Give the extent of all uninfected red blood cells.
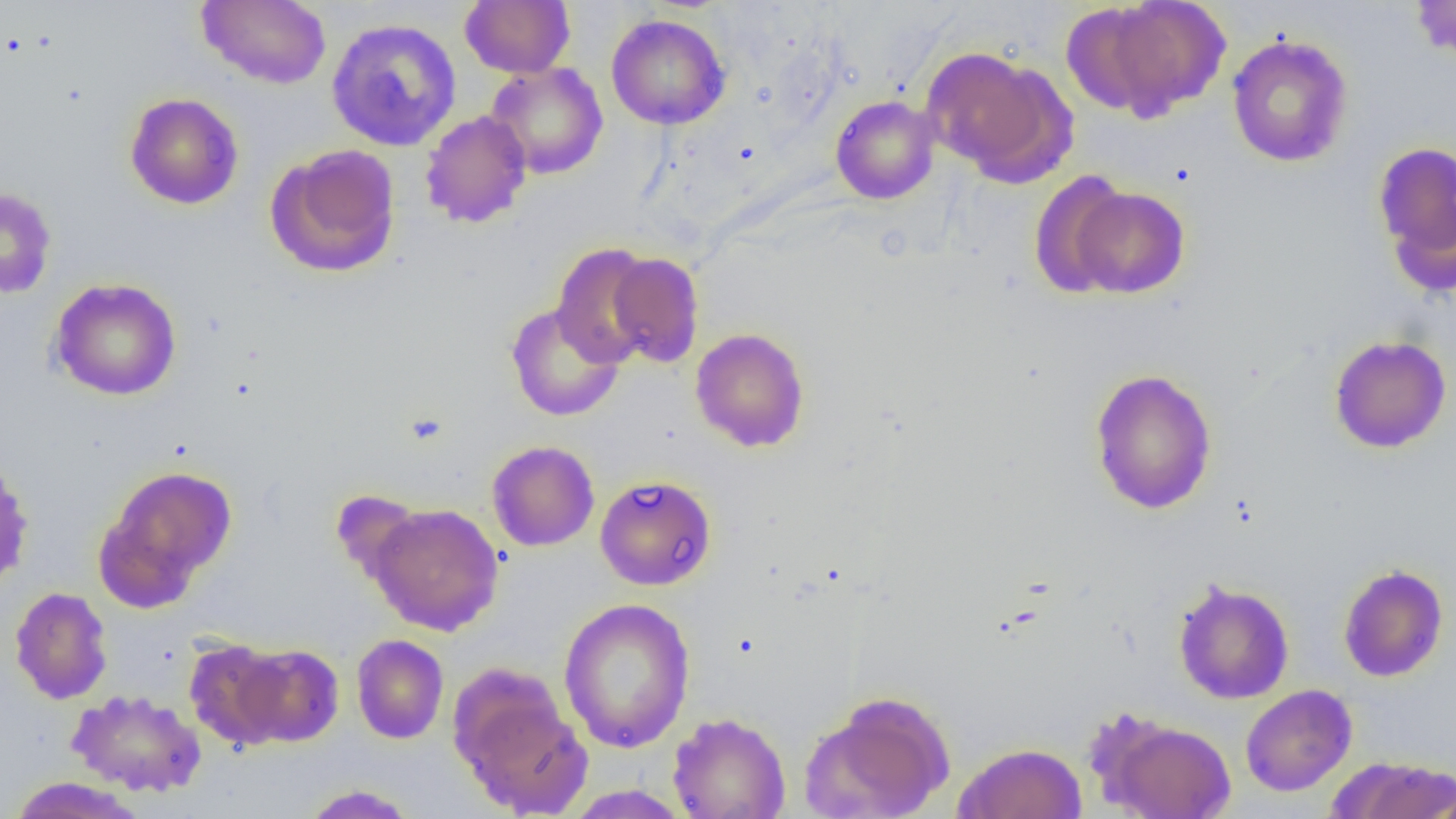
Approximate bounding boxes as (x1, y1, x2, y2) in pixels.
Uninfected red blood cells: (197, 0, 331, 89), (460, 0, 575, 78), (1081, 0, 1233, 121), (1410, 0, 1456, 63), (606, 14, 731, 130), (326, 17, 462, 151), (1226, 33, 1354, 168), (921, 46, 1073, 184), (485, 62, 608, 180), (125, 92, 243, 210), (830, 95, 940, 205), (420, 110, 532, 228), (1372, 139, 1456, 291), (266, 144, 402, 278), (1029, 171, 1135, 299), (1068, 186, 1190, 298), (0, 187, 57, 299), (551, 243, 660, 367), (603, 251, 705, 368), (49, 277, 182, 401), (505, 301, 625, 422), (690, 327, 810, 453), (1328, 335, 1452, 454), (1089, 367, 1217, 515), (487, 440, 600, 551), (0, 459, 34, 592), (95, 464, 237, 609), (594, 474, 717, 591), (330, 489, 431, 594), (367, 503, 504, 635), (1338, 563, 1449, 682), (1173, 579, 1295, 705), (10, 587, 113, 705), (558, 598, 696, 753), (352, 635, 449, 744), (184, 638, 291, 750), (232, 643, 344, 747), (454, 679, 593, 818), (1240, 684, 1357, 796), (67, 689, 207, 797), (802, 690, 956, 819), (668, 712, 791, 819), (1097, 714, 1237, 819), (952, 742, 1088, 819), (1324, 756, 1456, 818), (7, 776, 146, 819), (301, 784, 419, 818), (563, 785, 692, 818).

{
  "slide_level_diagnosis": "no evidence of blood parasites",
  "field_of_view": "single",
  "magnification": "1000x",
  "modality": "light microscopy",
  "image_size": "1456×819 pixels",
  "preparation": "thin blood smear"
}